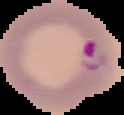
Image is 124×115 pixels. From a thin blood smear. Malaria status: parasitized. Cell region segmented out of the field of view; the surrounding area is masked to black.